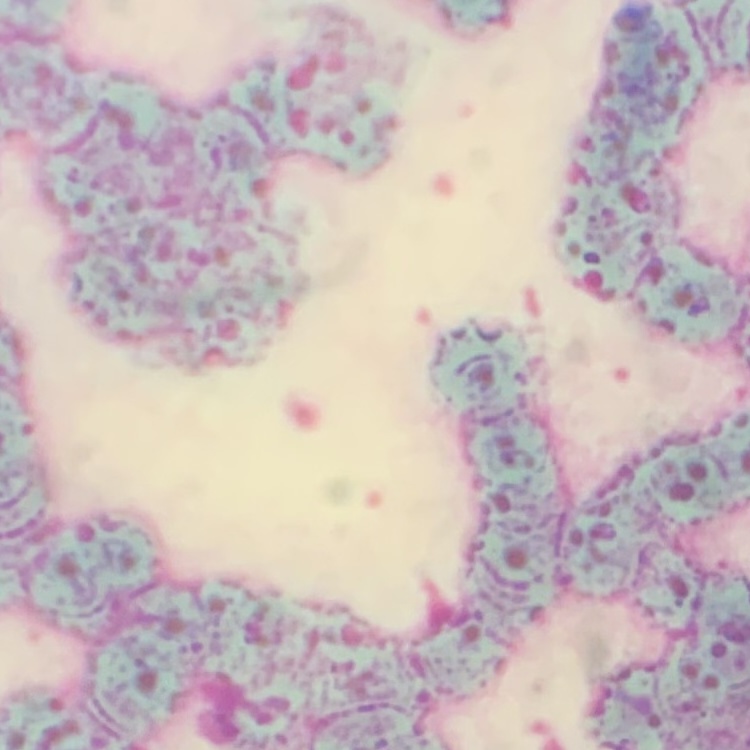

Summary:
  - Red blood cell morphology: rouleaux formation
  - Preparation: thin peripheral smear
  - Stain: Field's or Giemsa
  - Image type: square crop of a larger photomicrograph